Identify the parasite.
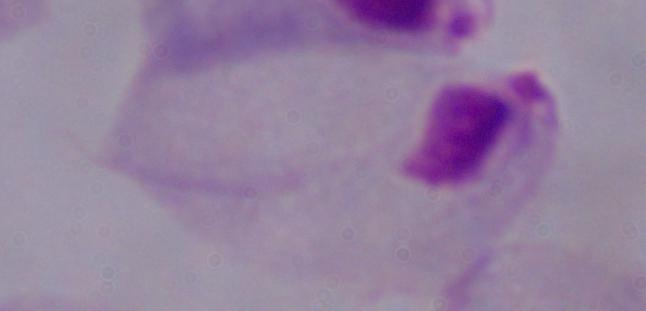
This is a trichomonad.

Captured at 1000x magnification. Photomicrograph.